Locate the P. falciparum-infected red blood cells and any of indeterminate infection status.
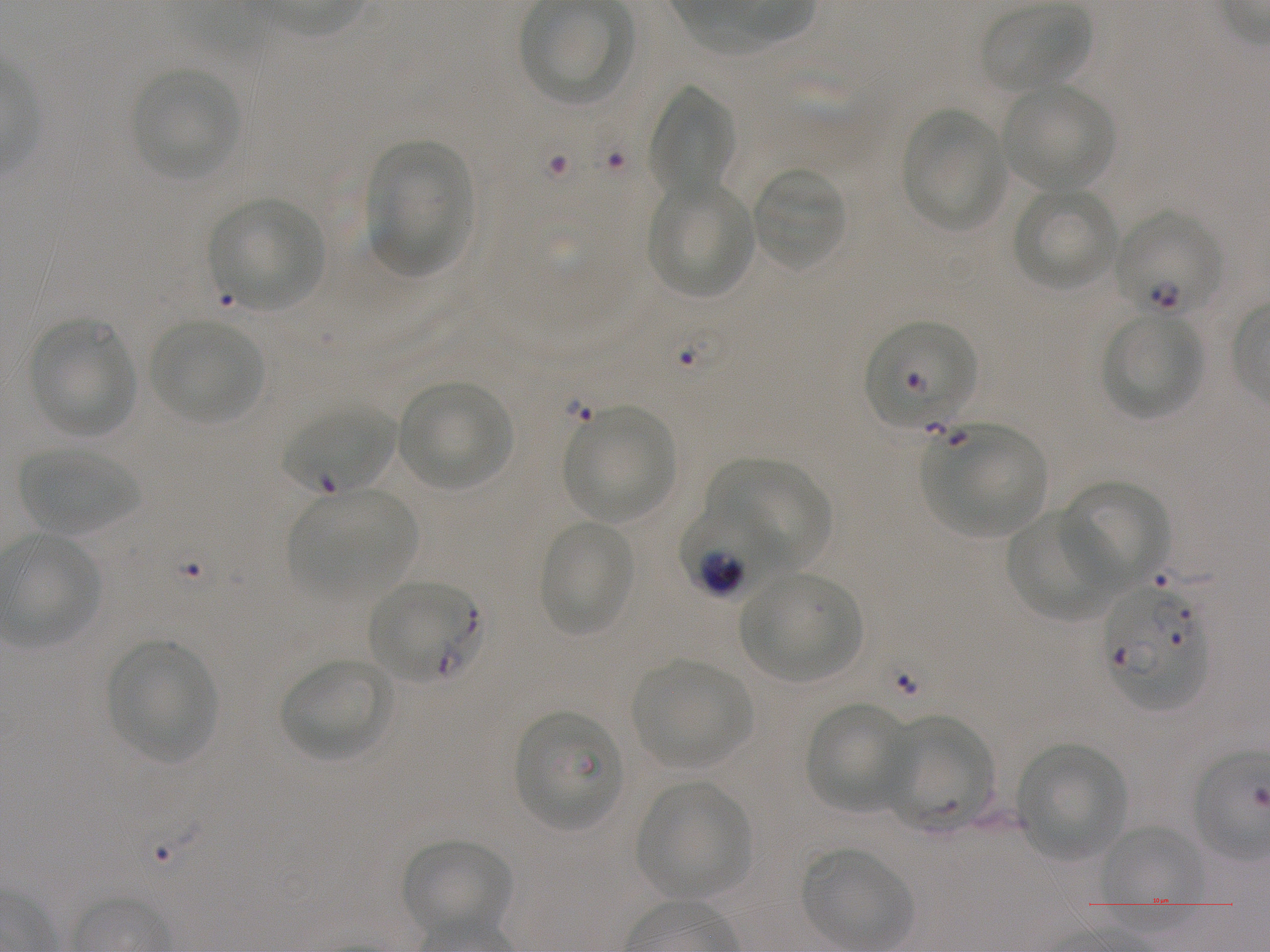

Approximate bounding boxes as (x1, y1, x2, y2) in pixels. Not every red blood cell is marked. A life-cycle stage — or a range of stages, where the recorded stages span more than one — follows each staged infected red blood cell.
Infected red blood cells: (1113, 210, 1224, 318) ring; (865, 321, 976, 428); (679, 502, 790, 600); (368, 581, 476, 682); (1102, 584, 1209, 710).
Red blood cells of indeterminate infection status: (285, 405, 395, 494), (512, 710, 623, 831).

Locations of uninfected red blood cells: (982, 3, 1090, 93), (129, 67, 241, 179), (1002, 83, 1114, 193), (651, 87, 734, 202), (902, 108, 1007, 231), (368, 138, 470, 277), (751, 167, 846, 271), (646, 180, 755, 298), (1015, 187, 1119, 292), (209, 199, 324, 310), (1103, 311, 1205, 419), (28, 319, 137, 438), (151, 320, 263, 424), (397, 380, 514, 489), (563, 406, 675, 522), (926, 422, 1047, 537), (20, 447, 137, 536), (712, 459, 829, 570), (1059, 479, 1171, 589), (296, 489, 418, 590), (1006, 508, 1121, 619), (537, 521, 635, 637), (739, 572, 862, 682), (107, 639, 216, 761), (282, 658, 390, 762), (631, 659, 750, 769), (805, 702, 914, 814), (880, 716, 995, 834), (1016, 743, 1126, 860), (635, 781, 750, 900), (1099, 824, 1203, 929), (402, 838, 510, 938), (802, 848, 909, 948). 100x objective under oil immersion, numerical aperture 1.25. Giemsa stain. Donor blood group A+. Thin blood smear. Static in-vitro culture of P. falciparum strain NF54. One field from this slide. Image is 1270×952 pixels.